Give the extent of all Plasmodium ovale-infected red blood cells.
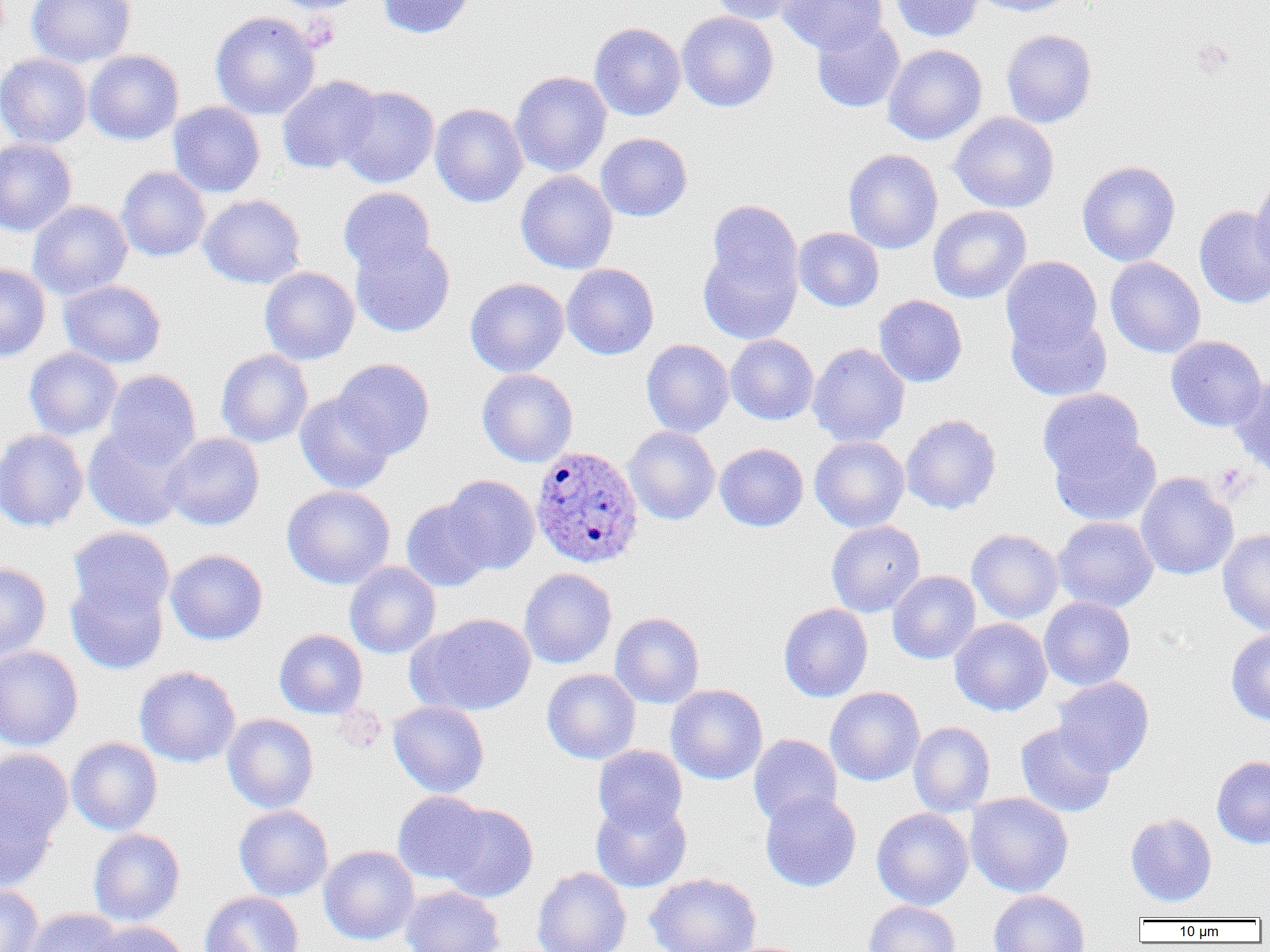
Approximate bounding boxes as named x1/y1/x2/y2 corners in pixels.
Plasmodium ovale-infected red blood cells: (x1=530, y1=445, x2=645, y2=568).

slide-level diagnosis = Plasmodium ovale
magnification = 1000x
preparation = thin blood smear
uninfected red blood cell locations = approximate bounding boxes as named x1/y1/x2/y2 corners in pixels: (x1=27, y1=0, x2=136, y2=68), (x1=270, y1=0, x2=370, y2=14), (x1=376, y1=0, x2=476, y2=39), (x1=708, y1=0, x2=809, y2=24), (x1=777, y1=0, x2=887, y2=55), (x1=889, y1=0, x2=984, y2=42), (x1=971, y1=0, x2=1079, y2=17), (x1=210, y1=11, x2=321, y2=120), (x1=677, y1=11, x2=778, y2=112), (x1=811, y1=19, x2=905, y2=113), (x1=589, y1=22, x2=686, y2=121), (x1=1001, y1=29, x2=1097, y2=128), (x1=883, y1=44, x2=987, y2=145), (x1=84, y1=50, x2=183, y2=146), (x1=0, y1=53, x2=91, y2=149), (x1=510, y1=71, x2=612, y2=177), (x1=277, y1=75, x2=381, y2=175), (x1=337, y1=85, x2=440, y2=187), (x1=168, y1=101, x2=265, y2=198), (x1=430, y1=103, x2=528, y2=208), (x1=949, y1=112, x2=1059, y2=213), (x1=595, y1=133, x2=692, y2=222), (x1=0, y1=139, x2=77, y2=237), (x1=843, y1=148, x2=943, y2=254), (x1=1077, y1=160, x2=1180, y2=266), (x1=116, y1=166, x2=211, y2=262), (x1=515, y1=170, x2=618, y2=274), (x1=1250, y1=176, x2=1270, y2=278), (x1=338, y1=187, x2=436, y2=276), (x1=198, y1=194, x2=305, y2=289), (x1=707, y1=199, x2=802, y2=299), (x1=27, y1=200, x2=132, y2=301), (x1=928, y1=205, x2=1031, y2=304), (x1=1194, y1=205, x2=1270, y2=309), (x1=793, y1=227, x2=884, y2=312), (x1=350, y1=235, x2=455, y2=337), (x1=697, y1=244, x2=801, y2=344), (x1=1001, y1=256, x2=1103, y2=358), (x1=1105, y1=256, x2=1206, y2=358), (x1=0, y1=263, x2=51, y2=362), (x1=561, y1=263, x2=659, y2=360), (x1=259, y1=266, x2=359, y2=365), (x1=465, y1=277, x2=569, y2=378), (x1=58, y1=279, x2=166, y2=369), (x1=874, y1=295, x2=967, y2=388), (x1=1006, y1=309, x2=1112, y2=401), (x1=725, y1=334, x2=819, y2=425), (x1=1165, y1=336, x2=1267, y2=431), (x1=641, y1=339, x2=734, y2=438), (x1=808, y1=342, x2=910, y2=448), (x1=24, y1=347, x2=122, y2=440), (x1=216, y1=349, x2=313, y2=447), (x1=333, y1=358, x2=434, y2=458), (x1=477, y1=368, x2=578, y2=467), (x1=103, y1=369, x2=201, y2=468), (x1=1229, y1=373, x2=1270, y2=477), (x1=1037, y1=389, x2=1145, y2=482), (x1=295, y1=392, x2=396, y2=494), (x1=901, y1=413, x2=1001, y2=514), (x1=83, y1=425, x2=190, y2=531), (x1=623, y1=427, x2=720, y2=525), (x1=0, y1=428, x2=89, y2=533), (x1=1050, y1=431, x2=1161, y2=528), (x1=162, y1=432, x2=265, y2=531), (x1=810, y1=436, x2=909, y2=532), (x1=715, y1=443, x2=808, y2=532), (x1=1135, y1=471, x2=1239, y2=581), (x1=443, y1=474, x2=540, y2=574), (x1=282, y1=485, x2=395, y2=589), (x1=400, y1=498, x2=493, y2=592), (x1=1053, y1=517, x2=1158, y2=612), (x1=826, y1=520, x2=925, y2=617), (x1=67, y1=526, x2=174, y2=624), (x1=967, y1=529, x2=1063, y2=624), (x1=1218, y1=529, x2=1270, y2=635), (x1=165, y1=549, x2=268, y2=645), (x1=344, y1=561, x2=441, y2=659), (x1=0, y1=562, x2=52, y2=664), (x1=519, y1=568, x2=617, y2=669), (x1=887, y1=571, x2=981, y2=664), (x1=66, y1=575, x2=169, y2=675), (x1=1039, y1=597, x2=1135, y2=690), (x1=778, y1=603, x2=873, y2=702), (x1=610, y1=612, x2=704, y2=708), (x1=409, y1=613, x2=537, y2=716), (x1=950, y1=618, x2=1052, y2=716), (x1=274, y1=629, x2=368, y2=719), (x1=1226, y1=629, x2=1270, y2=726), (x1=0, y1=645, x2=84, y2=751), (x1=134, y1=665, x2=241, y2=768), (x1=542, y1=669, x2=640, y2=764), (x1=1051, y1=676, x2=1154, y2=776), (x1=666, y1=684, x2=768, y2=785), (x1=825, y1=686, x2=925, y2=786), (x1=388, y1=701, x2=490, y2=798), (x1=222, y1=713, x2=319, y2=813), (x1=908, y1=721, x2=995, y2=816), (x1=1015, y1=722, x2=1116, y2=818), (x1=748, y1=734, x2=842, y2=827), (x1=67, y1=737, x2=163, y2=836), (x1=592, y1=745, x2=688, y2=833), (x1=0, y1=748, x2=73, y2=848), (x1=1212, y1=755, x2=1270, y2=848), (x1=392, y1=790, x2=490, y2=884), (x1=760, y1=791, x2=861, y2=892), (x1=964, y1=793, x2=1073, y2=897), (x1=0, y1=797, x2=58, y2=893), (x1=591, y1=797, x2=691, y2=893), (x1=438, y1=803, x2=538, y2=902), (x1=234, y1=805, x2=333, y2=901), (x1=871, y1=808, x2=974, y2=910), (x1=1125, y1=813, x2=1216, y2=906), (x1=88, y1=828, x2=185, y2=926), (x1=318, y1=845, x2=420, y2=944), (x1=532, y1=866, x2=632, y2=952), (x1=645, y1=873, x2=762, y2=952), (x1=0, y1=884, x2=43, y2=952), (x1=400, y1=885, x2=506, y2=952), (x1=988, y1=890, x2=1089, y2=952), (x1=199, y1=891, x2=304, y2=952), (x1=863, y1=900, x2=961, y2=952), (x1=24, y1=908, x2=123, y2=952), (x1=89, y1=920, x2=190, y2=952)
platelet locations = approximate bounding boxes as named x1/y1/x2/y2 corners in pixels: (x1=1213, y1=463, x2=1250, y2=499)
image size = 1270×952 pixels
modality = light microscopy
field of view = one of a larger specimen